Outline each uninfected red blood cell.
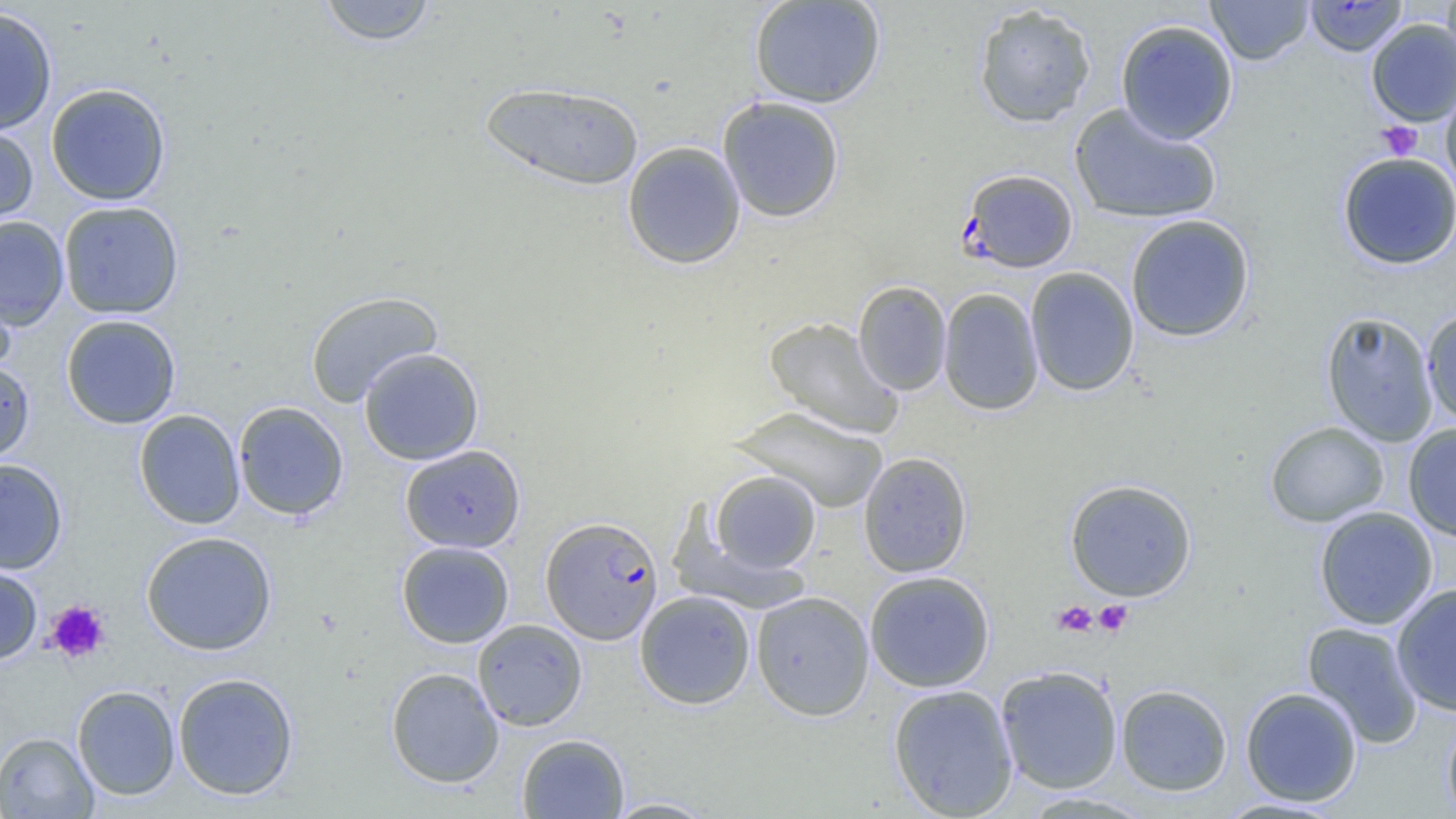

Approximate bounding boxes as named x1/y1/x2/y2 corners in pixels.
Uninfected red blood cells (subset): (x1=316, y1=0, x2=439, y2=46), (x1=748, y1=0, x2=886, y2=109), (x1=1205, y1=0, x2=1314, y2=65), (x1=1442, y1=0, x2=1456, y2=72), (x1=973, y1=3, x2=1097, y2=128), (x1=0, y1=6, x2=58, y2=135), (x1=1115, y1=19, x2=1239, y2=144), (x1=1366, y1=19, x2=1456, y2=126), (x1=480, y1=81, x2=645, y2=191), (x1=1441, y1=82, x2=1456, y2=199), (x1=46, y1=83, x2=171, y2=205), (x1=717, y1=96, x2=845, y2=223), (x1=1069, y1=103, x2=1222, y2=225), (x1=0, y1=121, x2=39, y2=229), (x1=622, y1=141, x2=746, y2=269), (x1=1337, y1=152, x2=1456, y2=270), (x1=58, y1=200, x2=184, y2=319), (x1=1125, y1=213, x2=1255, y2=342), (x1=0, y1=216, x2=69, y2=330), (x1=1025, y1=266, x2=1139, y2=397), (x1=0, y1=275, x2=17, y2=380), (x1=853, y1=280, x2=952, y2=395), (x1=938, y1=287, x2=1044, y2=416), (x1=305, y1=291, x2=443, y2=407), (x1=1421, y1=308, x2=1456, y2=426), (x1=1320, y1=311, x2=1439, y2=447), (x1=61, y1=314, x2=181, y2=429), (x1=763, y1=316, x2=904, y2=439), (x1=358, y1=347, x2=484, y2=466), (x1=0, y1=358, x2=35, y2=464), (x1=233, y1=401, x2=349, y2=520), (x1=732, y1=406, x2=888, y2=513), (x1=134, y1=409, x2=245, y2=529), (x1=1264, y1=421, x2=1389, y2=527), (x1=1403, y1=422, x2=1456, y2=541), (x1=399, y1=445, x2=526, y2=553), (x1=858, y1=451, x2=973, y2=578), (x1=0, y1=458, x2=68, y2=574), (x1=710, y1=470, x2=821, y2=574), (x1=1064, y1=478, x2=1197, y2=601), (x1=1313, y1=506, x2=1439, y2=630), (x1=141, y1=531, x2=277, y2=655), (x1=396, y1=541, x2=514, y2=648), (x1=0, y1=560, x2=43, y2=665), (x1=864, y1=570, x2=995, y2=692), (x1=1391, y1=582, x2=1456, y2=717), (x1=634, y1=590, x2=756, y2=709), (x1=751, y1=591, x2=875, y2=720), (x1=473, y1=619, x2=588, y2=731), (x1=1302, y1=621, x2=1424, y2=749), (x1=995, y1=665, x2=1123, y2=794), (x1=386, y1=667, x2=504, y2=788), (x1=172, y1=672, x2=300, y2=800), (x1=887, y1=684, x2=1018, y2=818), (x1=1115, y1=684, x2=1233, y2=796), (x1=72, y1=685, x2=180, y2=801), (x1=1240, y1=686, x2=1363, y2=807), (x1=1442, y1=713, x2=1456, y2=819), (x1=0, y1=732, x2=98, y2=819), (x1=516, y1=733, x2=629, y2=818), (x1=602, y1=797, x2=721, y2=818), (x1=1214, y1=797, x2=1346, y2=818).

Platelet locations: (x1=1377, y1=121, x2=1422, y2=161), (x1=45, y1=599, x2=111, y2=664), (x1=1093, y1=599, x2=1133, y2=637), (x1=1052, y1=600, x2=1097, y2=637). Plasmodium falciparum-infected red blood cell locations (subset): (x1=960, y1=168, x2=1079, y2=273), (x1=541, y1=516, x2=663, y2=645). Slide-level diagnosis: Plasmodium falciparum. Optical microscopy. One field of a larger specimen. Thin blood smear. 1000x magnification. Image is 1456×819 pixels.